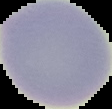

{
  "image_size": "112×109 pixels",
  "result": "no Plasmodium parasites seen",
  "preparation": "thin blood smear",
  "image_type": "segmented cell region on a black background"
}